Describe the morphology of the red blood cells.
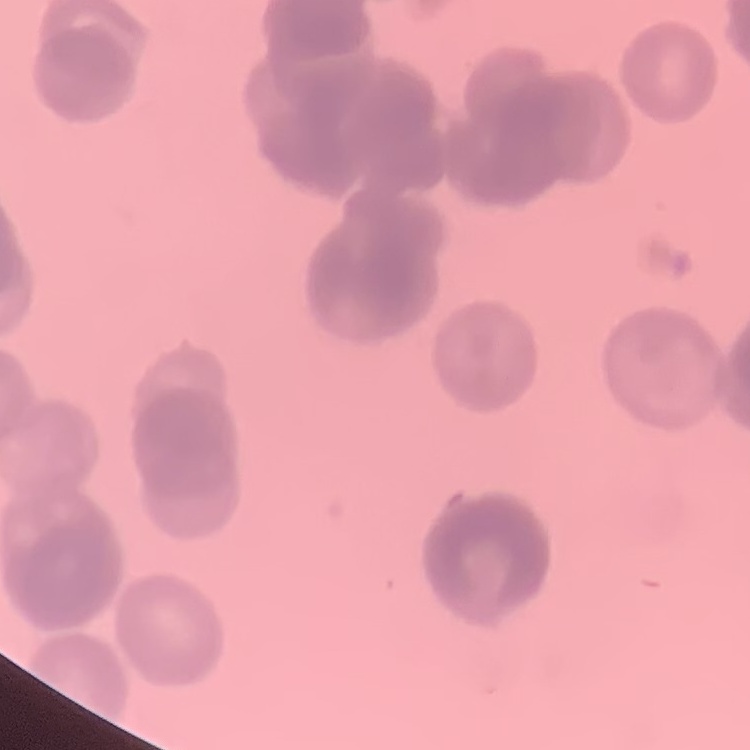

Rouleaux formation.

image type = one tile cut from a larger photomicrograph
stain = Field's or Giemsa
preparation = thin blood smear